Locate platelets.
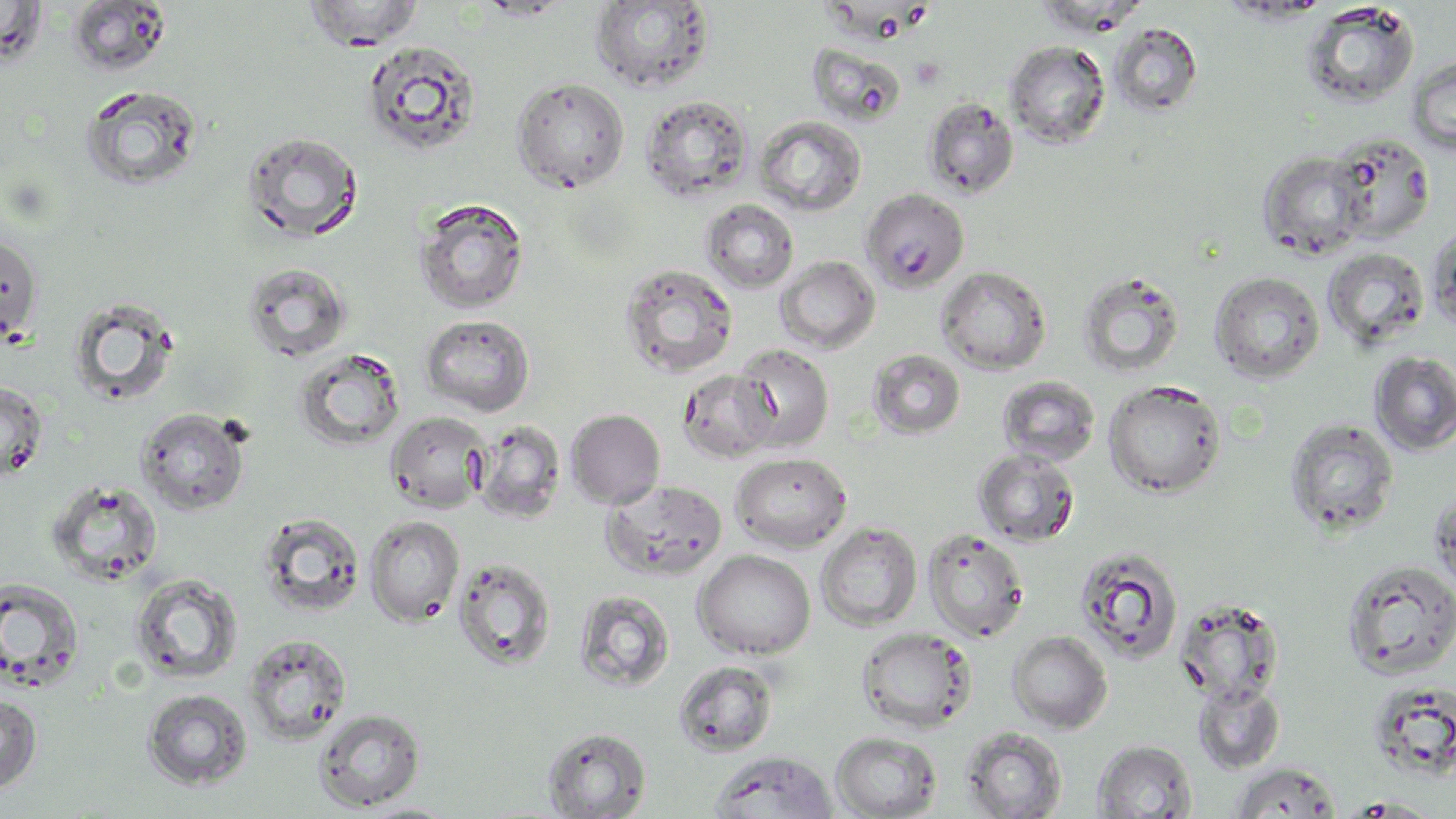
Approximate bounding boxes as [x1, y1, x2, y2] in pixels.
Platelets: [901, 2, 931, 28], [911, 57, 945, 90].

Uninfected red blood cell locations: [303, 0, 425, 51], [1, 1, 47, 68], [65, 1, 173, 77], [590, 1, 715, 93], [1034, 1, 1147, 37], [1301, 1, 1420, 109], [1109, 22, 1204, 118], [361, 40, 483, 159], [1004, 40, 1111, 149], [807, 42, 907, 128], [1405, 56, 1456, 156], [511, 77, 630, 193], [79, 84, 205, 192], [640, 94, 754, 202], [921, 96, 1020, 200], [755, 115, 867, 216], [241, 130, 365, 244], [1327, 132, 1435, 243], [1257, 150, 1370, 260], [860, 188, 970, 294], [412, 197, 530, 314], [701, 199, 799, 293], [1426, 225, 1456, 335], [0, 232, 43, 346], [1322, 248, 1429, 352], [774, 255, 880, 355], [242, 261, 352, 362], [619, 263, 739, 378], [936, 266, 1051, 374], [1076, 270, 1186, 378], [1209, 271, 1325, 384], [66, 296, 181, 408], [420, 314, 535, 416], [731, 343, 835, 452], [293, 347, 407, 452], [867, 349, 966, 439], [1370, 351, 1456, 455], [678, 369, 777, 464], [996, 375, 1101, 467], [0, 380, 48, 482], [1102, 380, 1227, 499], [136, 407, 250, 515], [565, 409, 666, 509], [385, 410, 492, 514], [1284, 417, 1400, 537], [472, 420, 567, 525], [972, 447, 1080, 547], [730, 452, 852, 553], [47, 479, 164, 586], [601, 479, 728, 581], [1430, 489, 1456, 597], [257, 512, 366, 618], [365, 515, 465, 625], [816, 522, 923, 632], [922, 527, 1030, 643], [1074, 546, 1184, 664], [693, 549, 815, 660], [452, 556, 558, 672], [1340, 559, 1456, 680], [129, 573, 244, 685], [0, 577, 86, 692], [574, 589, 675, 692], [1174, 598, 1284, 706], [855, 626, 978, 734], [1007, 630, 1112, 733], [243, 632, 352, 745], [673, 659, 779, 758], [1192, 679, 1285, 774], [1366, 681, 1456, 781], [142, 689, 253, 790], [0, 694, 42, 796], [314, 708, 426, 811], [541, 727, 651, 818], [961, 727, 1067, 818], [831, 731, 942, 819], [1092, 740, 1197, 818], [709, 751, 839, 818], [1230, 762, 1340, 818], [1338, 797, 1443, 817], [354, 801, 464, 818]. Slide-level diagnosis: no evidence of blood parasites. Single field of view. May-Grünwald-Giemsa-stained preparation. 1000x magnification. Optical microscopy. Thin blood film. Image is 1456×819 pixels.